Draw a bounding box around every Plasmodium parasite, every leukocyte, and every artifact (stain precipitate or debris).
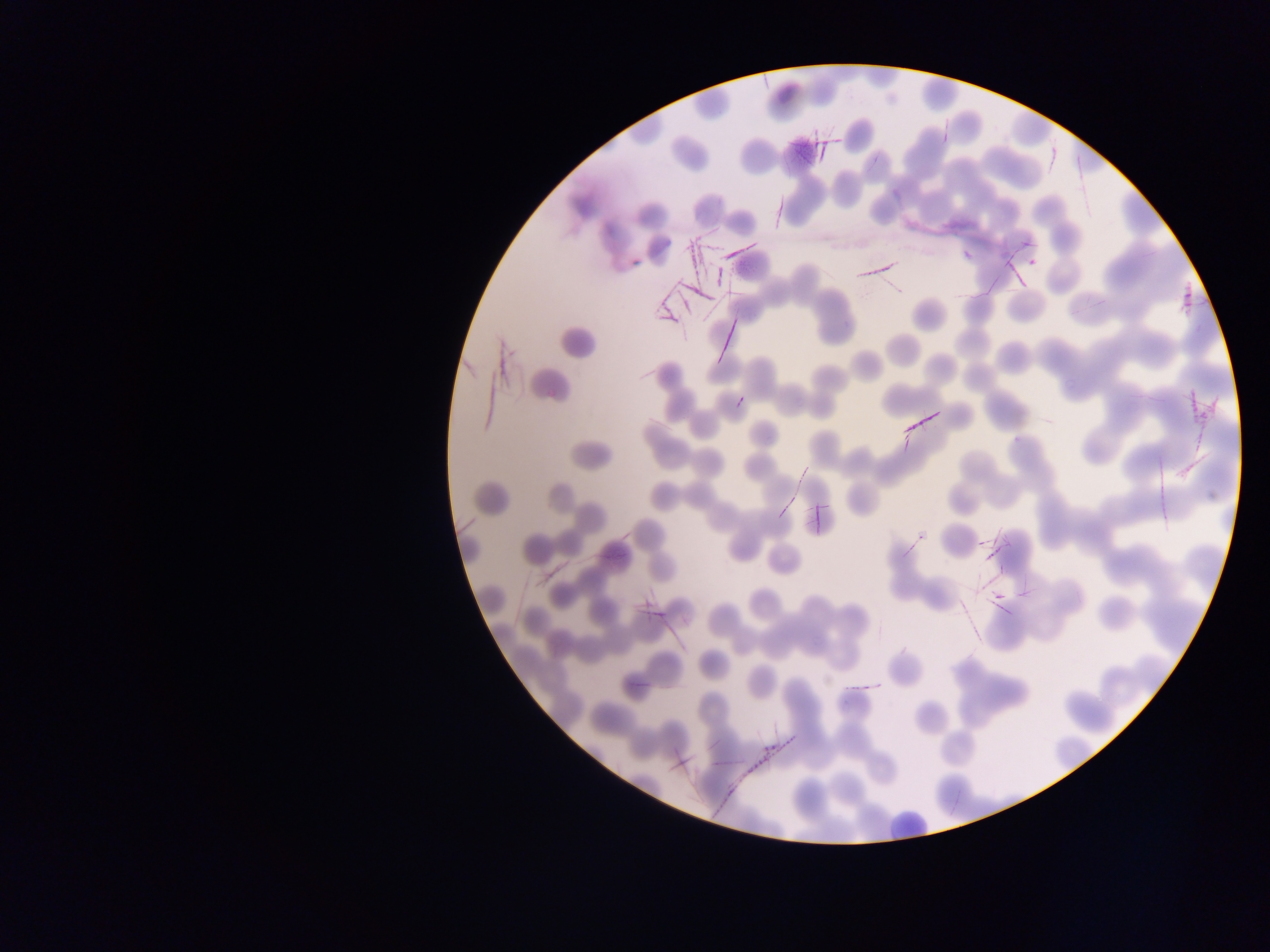

Approximate bounding boxes as left top right bottom in pixels.
No Plasmodium parasites observed.
Leukocytes: 887 802 932 847.
Artifacts (stain precipitate or debris): 791 135 833 166; 653 228 723 323; 857 257 901 285; 1174 286 1201 310; 712 308 742 363; 480 328 518 410; 1188 380 1227 420; 903 405 941 443; 791 445 820 497; 1172 455 1205 478; 804 486 841 533; 972 530 1011 581; 980 585 1011 611; 637 586 675 637; 630 674 652 693; 734 742 783 802; 671 747 697 775.

{
  "image_size": "1270×952 pixels",
  "field_of_view": "single",
  "capture": "mobile-phone photograph through a microscope",
  "country": "Ghana",
  "preparation": "thin blood smear"
}